Comment on the morphology of the red blood cells.
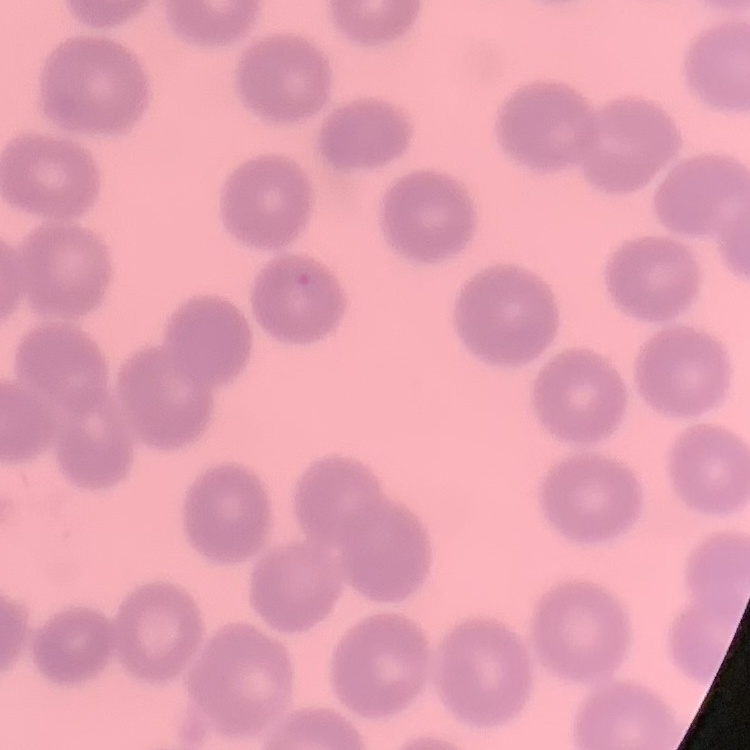

They show no rouleaux formation.

Summary:
  - Preparation: thin blood smear
  - Stain: Field's or Giemsa
  - Image type: one tile cut from a larger photomicrograph